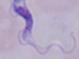 Captured at 1000x magnification. A trypanosome is shown. Micrograph.